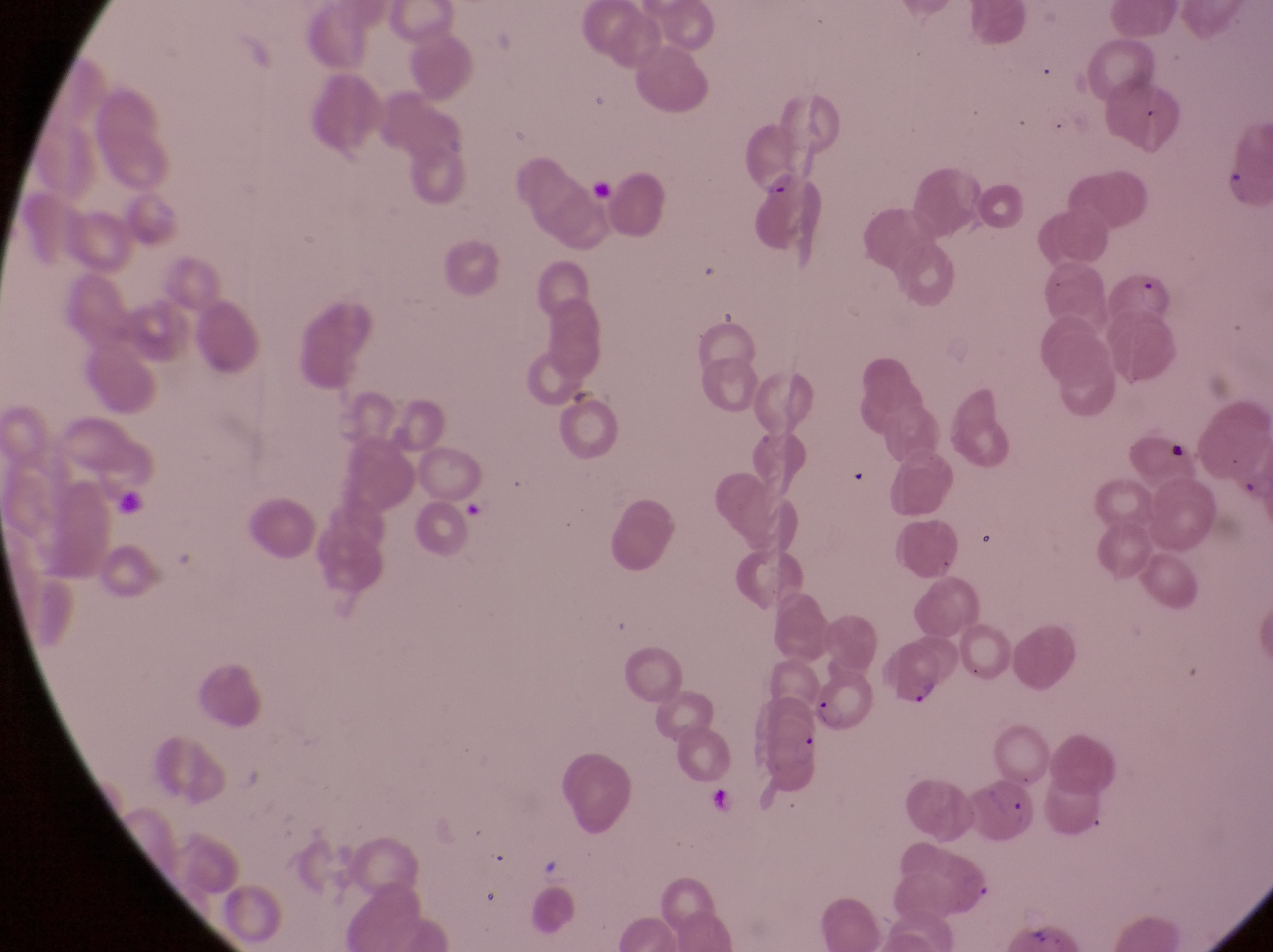 Approximate bounding boxes as {left, top, right, bottom} in pixels. Artifact (platelet-like body, stain precipitate, or debris) locations: {1166, 435, 1194, 467}. Parasitised red blood cell locations: {757, 174, 824, 266}, {1109, 267, 1179, 334}, {881, 640, 948, 712}, {811, 674, 873, 731}, {973, 777, 1048, 857}. Image is 1273×952 pixels. Collected in Uganda. Captured by a smartphone held over the eyepiece of an Olympus CX-23 microscope. Magnification of 1000x. Single field of view. Thin blood film.